Identify the blood parasite species.
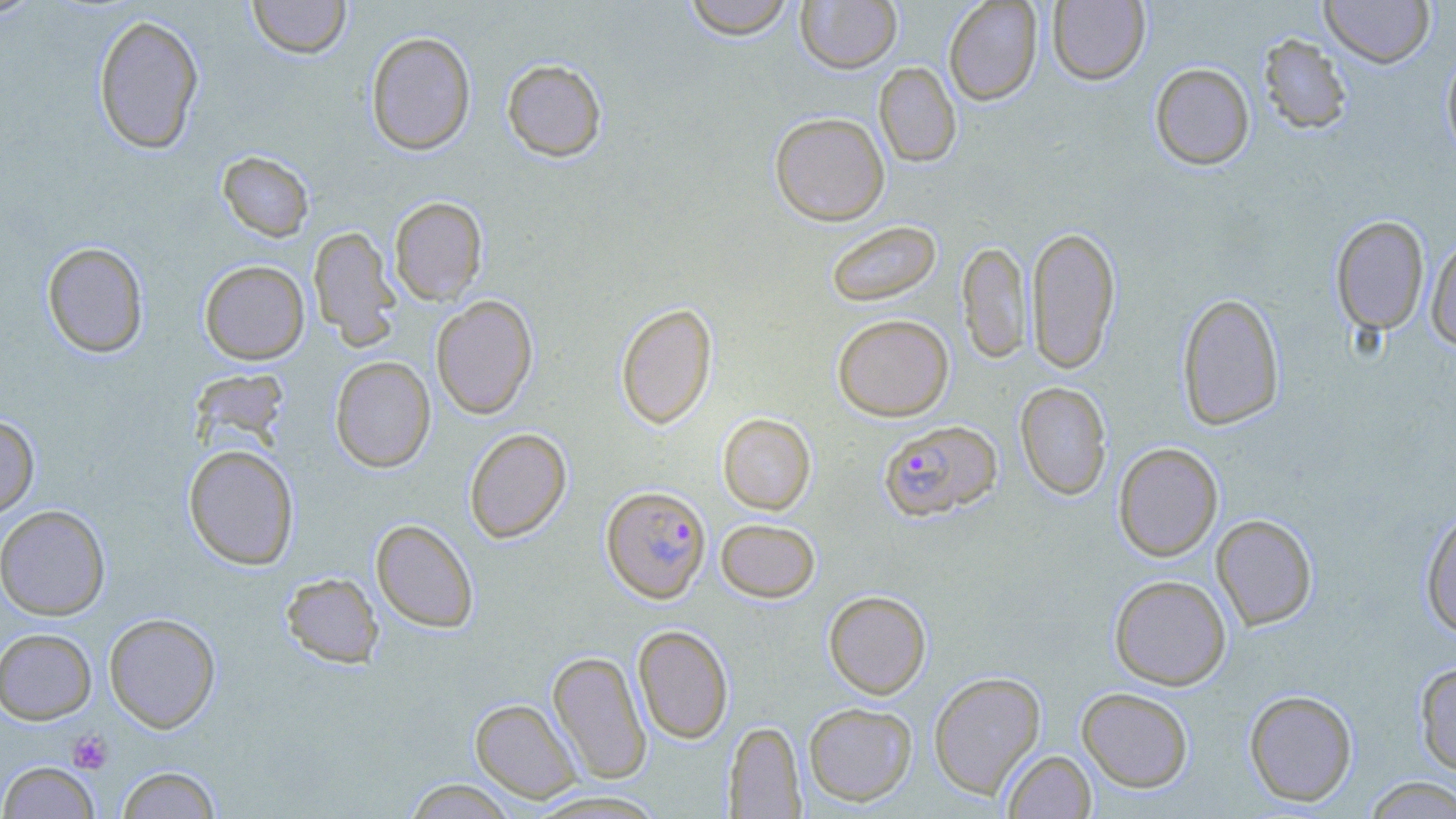
Plasmodium falciparum.

Approximate bounding boxes as (x1,y1)-(x2,y2) corner pairs in pixels. Uninfected red blood cell locations: (0,0)-(46,22), (247,0)-(352,59), (682,0)-(797,39), (795,0)-(902,74), (943,0)-(1043,105), (1320,0)-(1436,67), (1048,1)-(1149,85), (93,13)-(204,154), (365,31)-(476,155), (1258,33)-(1352,134), (1441,46)-(1456,162), (501,58)-(607,162), (874,61)-(961,167), (1149,62)-(1255,169), (769,112)-(890,226), (217,150)-(314,242), (388,196)-(488,305), (1330,215)-(1429,337), (825,220)-(942,308), (1026,225)-(1121,374), (309,226)-(401,350), (1427,233)-(1456,352), (957,240)-(1032,364), (42,241)-(149,358), (199,260)-(310,364), (1177,292)-(1285,430), (430,295)-(538,419), (615,302)-(717,429), (832,314)-(954,421), (330,356)-(436,473), (189,368)-(292,454), (1015,381)-(1112,500), (717,413)-(816,515), (0,414)-(39,520), (464,427)-(572,543), (1113,442)-(1223,561), (183,444)-(299,570), (0,504)-(110,620), (1420,508)-(1456,637), (1211,514)-(1318,629), (370,518)-(479,633), (716,518)-(821,603), (281,572)-(384,667), (1109,574)-(1232,690), (823,590)-(931,699), (103,612)-(221,733), (633,625)-(733,744), (0,627)-(97,724), (548,650)-(652,784), (1413,659)-(1456,776), (928,671)-(1046,798), (1076,687)-(1194,792), (1244,689)-(1358,807), (470,698)-(581,802), (803,702)-(917,806), (724,721)-(805,817), (1002,750)-(1096,818), (0,760)-(99,818), (116,765)-(221,819), (1363,776)-(1456,818), (402,778)-(519,818), (526,790)-(670,818). Platelet locations: (67,730)-(113,774). Plasmodium falciparum-infected red blood cell locations: (878,419)-(1002,521), (601,485)-(711,603). Image is 1456×819 pixels. Light microscopy. Thin blood smear. May-Grünwald-Giemsa stain. Single field of view. Captured at 1000x magnification.